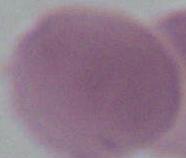
Photomicrograph. Captured at 1000x magnification. An erythrocyte is shown.